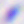
magnification = 400x
identification = Toxoplasma gondii
modality = micrograph